Report the malaria status of this cell.
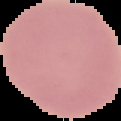

It is uninfected.

The area outside the segmented cell region is set to black. From a thin blood film. Image is 121×121 pixels.